Report the malaria status of this cell.
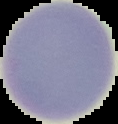
Uninfected.

Summary:
  - Preparation: thin blood smear
  - Image type: segmented cell region on a black background
  - Image size: 118×124 pixels